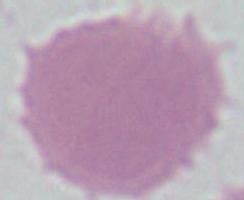

{
  "modality": "micrograph",
  "magnification": "1000x",
  "identification": "erythrocyte"
}